Report the malaria status of this cell.
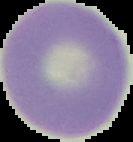

It is uninfected.

Summary:
  - Image type: segmented cell region with the area outside set to black
  - Preparation: thin blood film
  - Image size: 133×142 pixels